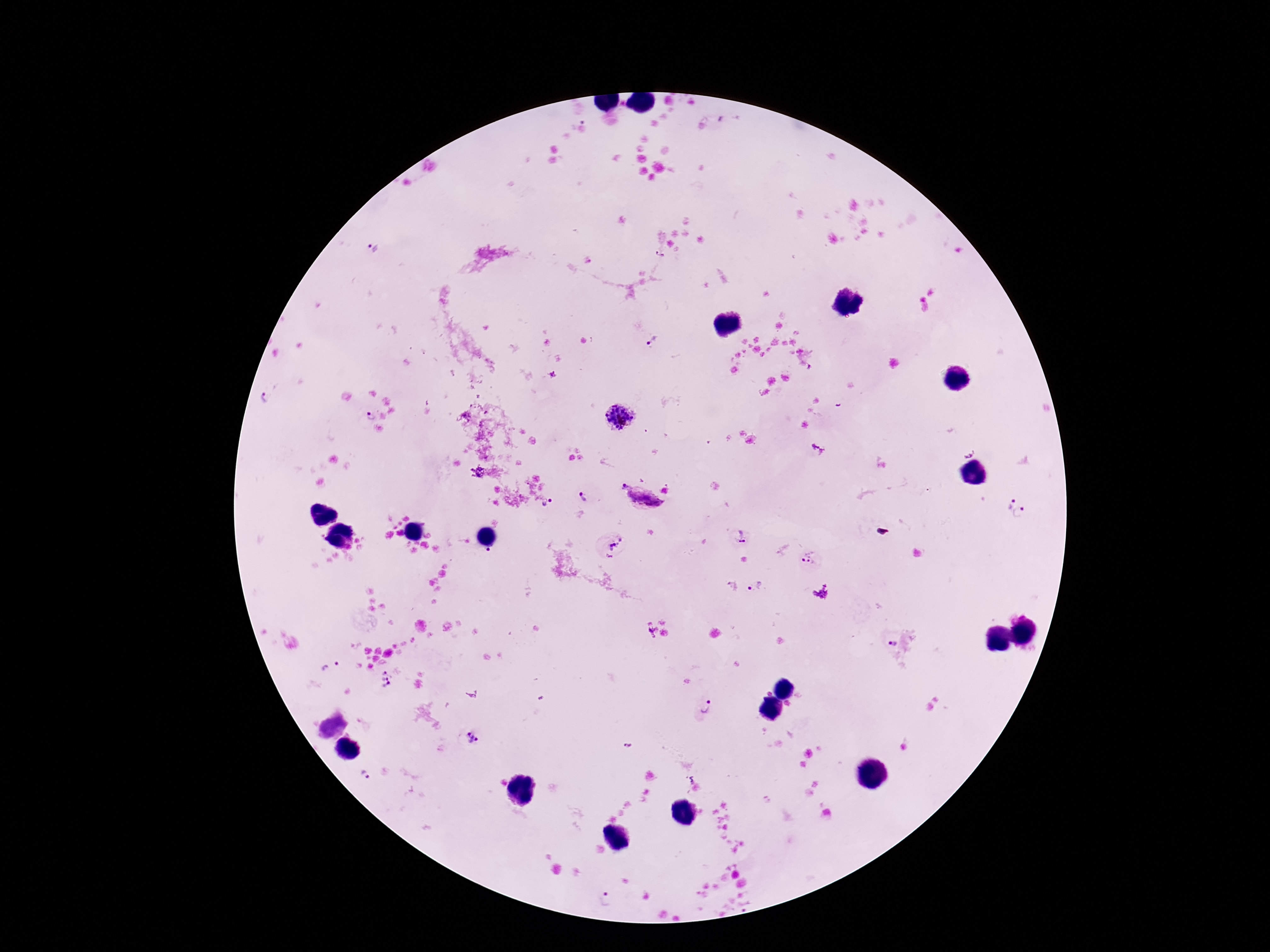

field_of_view: single
image_size: 1270×952 pixels
patient_malaria_status: positive
capture: smartphone camera through the microscope eyepiece
plasmodium_parasite_locations: 'approximate object centers, in pixels from the top-left corner: (x=374, y=248), (x=660, y=256), (x=653, y=341), (x=552, y=375), (x=267, y=397), (x=370, y=417), (x=617, y=419), (x=623, y=487), (x=666, y=490), (x=583, y=496), (x=644, y=499), (x=547, y=503), (x=1009, y=503), (x=1021, y=512), (x=741, y=537), (x=612, y=547), (x=488, y=550), (x=810, y=562), (x=756, y=587), (x=889, y=640), (x=330, y=666), (x=383, y=678), (x=704, y=707), (x=472, y=737), (x=628, y=746), (x=363, y=774), (x=605, y=900)'
stain: Giemsa
magnification: 100x
preparation: thick blood smear